State which cell type is depicted.
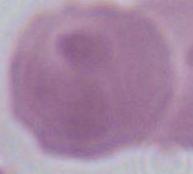
An erythrocyte.

Summary:
  - Modality: photomicrograph
  - Magnification: 1000x